Classify this cell by malaria status.
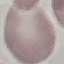
Uninfected.

capture: smartphone camera at the microscope eyepiece
preparation: thin smear
stain: Giemsa
image_type: cell patch, automatically extracted from a larger field of view and resized to 64 × 64 pixels